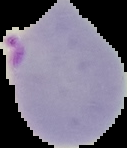

image type = segmented cell region on a black background
preparation = thin blood film
image size = 127×148 pixels
malaria status = parasitized